Name the parasite shown.
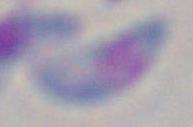

Toxoplasma gondii.

magnification: 1000x
modality: photomicrograph